Give the position of every Plasmodium parasite visible.
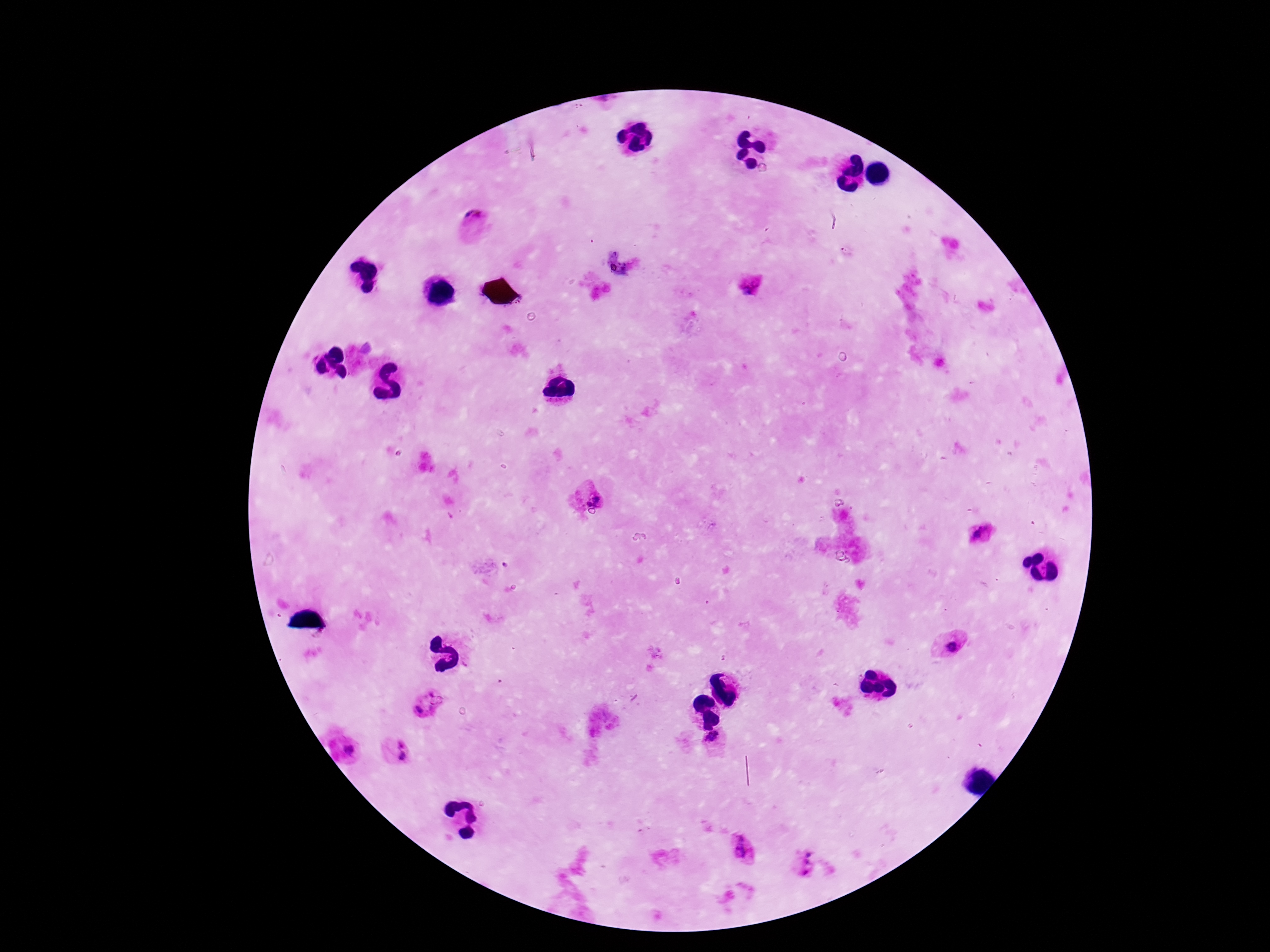

Approximate object centers, in pixels from the top-left corner.
Plasmodium parasites: (x=474, y=219), (x=748, y=283), (x=588, y=493), (x=978, y=533), (x=952, y=644), (x=427, y=706), (x=714, y=743), (x=350, y=750), (x=395, y=751), (x=745, y=850), (x=806, y=864).

Summary:
  - Field of view: single
  - Capture: smartphone camera through the microscope eyepiece
  - Stain: Giemsa
  - Preparation: thick blood film
  - Patient malaria status: infected
  - Image size: 1270×952 pixels
  - Magnification: 100x